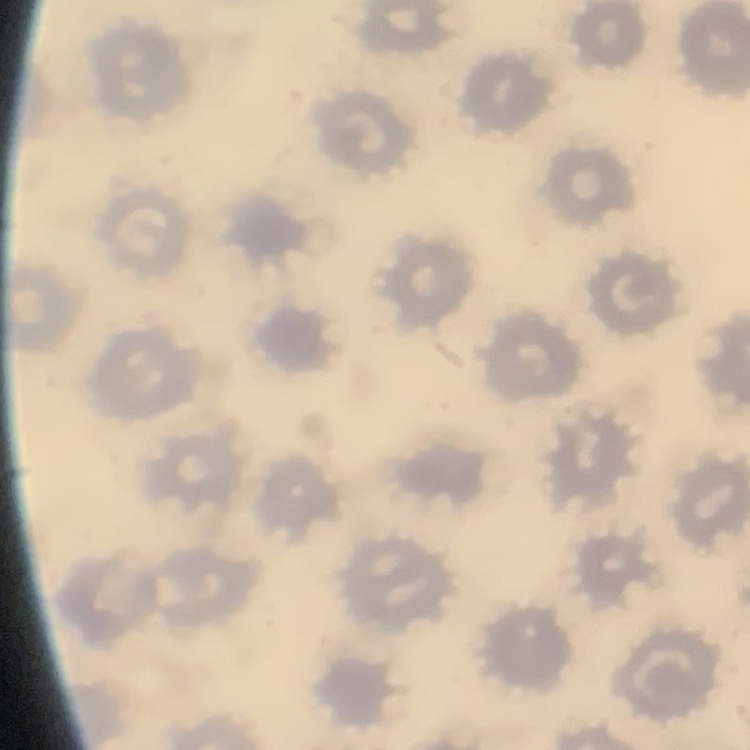

erythrocyte morphology = no rouleaux formation
preparation = thin peripheral smear
image type = square crop of a larger photomicrograph
stain = Field's or Giemsa